Classify this cell by malaria status.
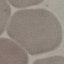

Uninfected.

Thin blood film. Giemsa-stained preparation. Photographed with a smartphone camera at the microscope eyepiece. Automatically extracted cell patch, resized to 64 × 64 pixels.